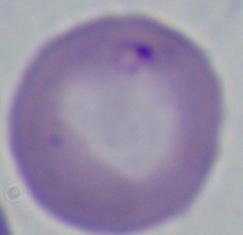
Summary:
  - Identification: Babesia
  - Modality: micrograph
  - Magnification: 1000x